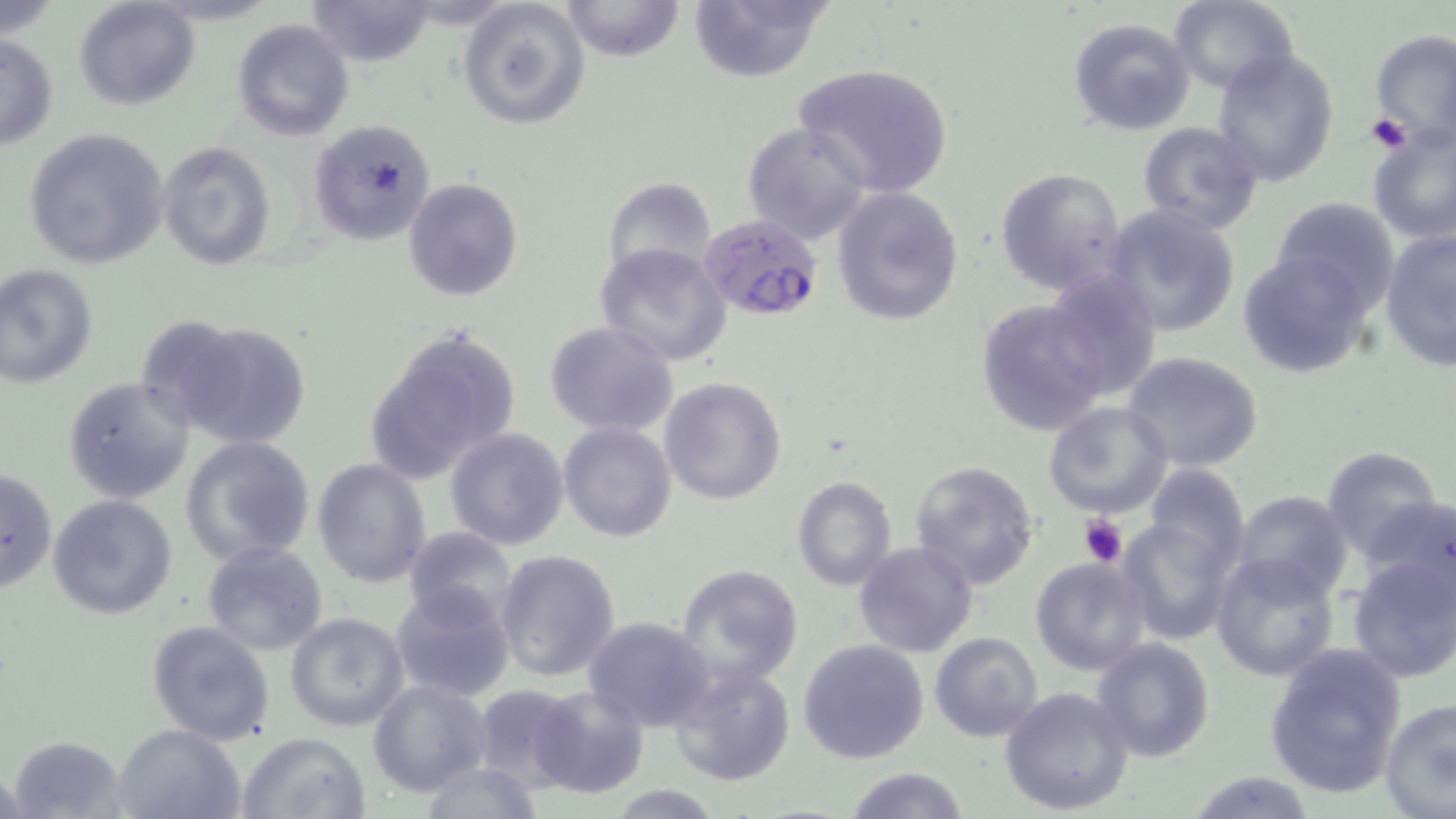
slide-level diagnosis = Plasmodium falciparum
image size = 1456×819 pixels
modality = light microscopy
preparation = thin blood film
platelet locations = approximate bounding boxes as (x1, y1, x2, y2) in pixels: (1367, 113, 1410, 154), (1077, 514, 1129, 568)
magnification = 1000x
Plasmodium falciparum-infected red blood cell locations = approximate bounding boxes as (x1, y1, x2, y2) in pixels: (699, 215, 824, 322)
uninfected red blood cell locations = approximate bounding boxes as (x1, y1, x2, y2) in pixels: (0, 0, 60, 44), (74, 0, 199, 112), (306, 0, 439, 68), (559, 0, 685, 62), (1169, 0, 1298, 96), (458, 1, 589, 130), (685, 1, 834, 83), (1067, 16, 1197, 137), (231, 19, 352, 141), (1368, 29, 1456, 151), (0, 32, 59, 154), (1210, 46, 1341, 186), (792, 62, 954, 198), (307, 119, 437, 246), (742, 121, 873, 244), (1135, 121, 1266, 235), (23, 126, 170, 271), (1367, 127, 1456, 246), (157, 141, 276, 272), (995, 167, 1126, 296), (404, 177, 523, 301), (602, 178, 717, 280), (832, 185, 964, 325), (1271, 196, 1400, 315), (1102, 204, 1242, 339), (1380, 227, 1456, 372), (595, 244, 731, 368), (1236, 247, 1373, 378), (0, 264, 99, 388), (1042, 268, 1163, 402), (976, 298, 1110, 437), (154, 315, 313, 450), (363, 322, 522, 485), (543, 322, 679, 437), (1119, 351, 1265, 474), (62, 376, 195, 503), (658, 377, 787, 505), (1043, 401, 1172, 518), (559, 421, 679, 542), (444, 428, 570, 550), (177, 435, 316, 566), (1320, 445, 1447, 560), (312, 457, 432, 589), (909, 460, 1042, 589), (1141, 463, 1251, 577), (1, 464, 57, 596), (792, 476, 896, 592), (1230, 491, 1352, 603), (47, 493, 179, 621), (1358, 495, 1455, 596), (1117, 517, 1234, 643), (403, 525, 516, 629), (202, 541, 328, 656), (853, 542, 980, 658), (495, 550, 620, 684), (1211, 550, 1341, 681), (1345, 550, 1456, 682), (1030, 556, 1154, 676), (675, 564, 804, 687), (390, 584, 515, 703), (285, 611, 411, 732), (583, 616, 714, 731), (147, 618, 276, 744), (930, 633, 1043, 742), (1090, 636, 1216, 762), (797, 639, 930, 765), (1263, 641, 1406, 800), (668, 662, 796, 787), (369, 677, 492, 798), (468, 684, 588, 792), (529, 684, 650, 799), (999, 685, 1135, 815), (1380, 698, 1456, 817), (113, 722, 245, 819), (237, 732, 370, 818), (7, 735, 128, 818), (419, 760, 545, 817), (846, 767, 970, 819), (1186, 771, 1319, 817), (604, 785, 726, 816)
field of view = one of a larger specimen
stain = May-Grünwald-Giemsa